Locate every blood parasite and identify its species.
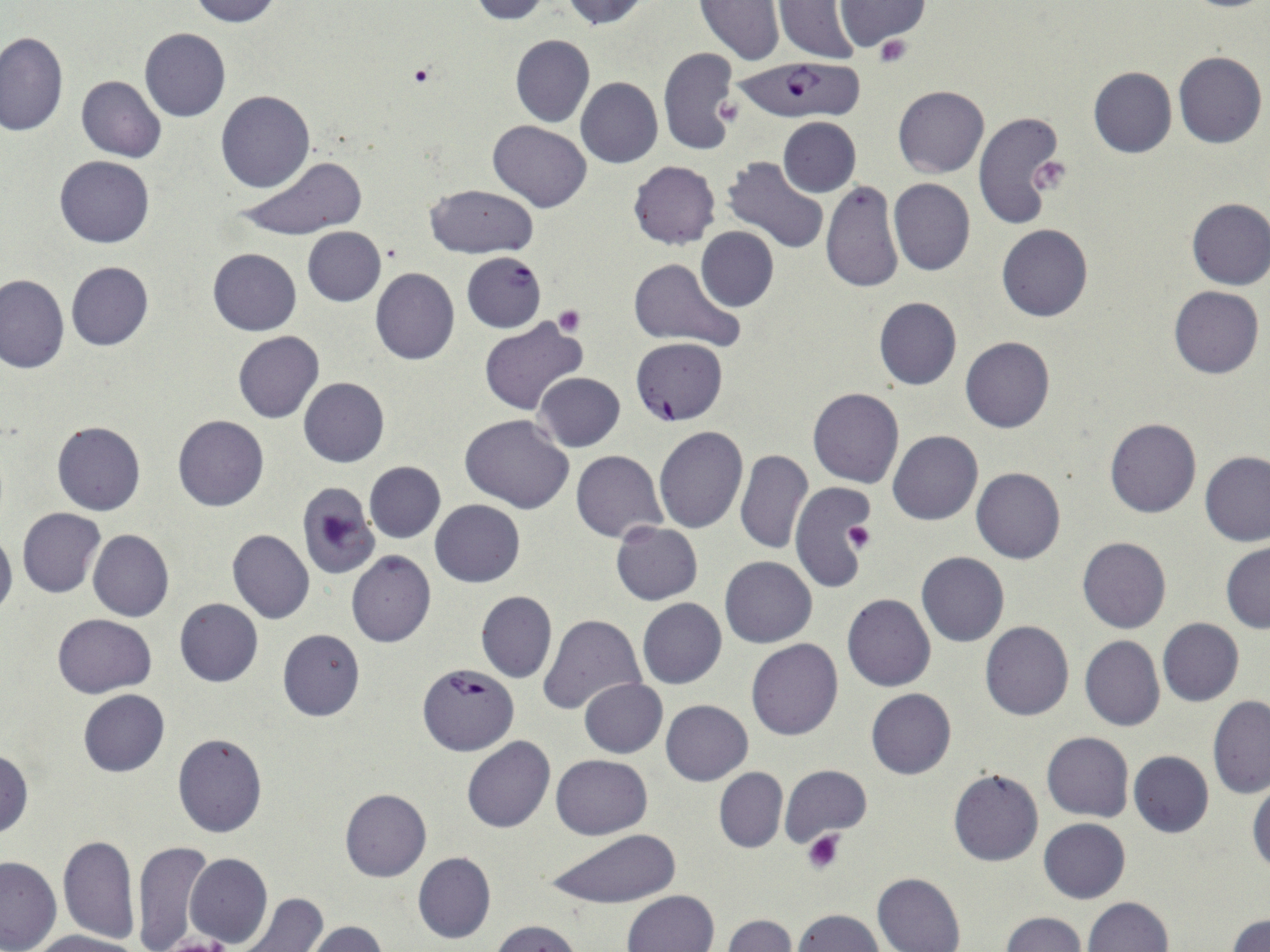
Approximate bounding boxes as (x1, y1, x2, y2) in pixels.
Plasmodium falciparum-infected red blood cells: (733, 57, 869, 131), (462, 251, 546, 333), (631, 337, 727, 425), (420, 665, 517, 754).
No Plasmodium ovale, Plasmodium malariae, Plasmodium vivax, Babesia divergens, or Trypanosoma brucei observed.

Summary:
  - Platelet locations: (875, 33, 914, 68), (407, 64, 439, 89), (1033, 157, 1071, 194), (554, 306, 586, 336), (845, 521, 877, 553), (802, 829, 844, 874), (165, 936, 231, 952)
  - White blood cell locations: (295, 481, 381, 578)
  - Uninfected red blood cell locations: (187, 0, 279, 25), (469, 0, 553, 23), (559, 0, 652, 28), (774, 0, 862, 65), (835, 0, 933, 50), (696, 1, 784, 64), (140, 29, 231, 122), (0, 31, 68, 136), (511, 34, 594, 128), (658, 46, 739, 157), (1173, 50, 1267, 148), (1087, 65, 1176, 158), (76, 76, 165, 161), (576, 77, 664, 169), (893, 85, 988, 178), (216, 90, 314, 192), (972, 109, 1068, 229), (778, 117, 861, 196), (487, 120, 592, 211), (234, 154, 365, 244), (54, 156, 155, 248), (723, 156, 829, 255), (627, 161, 720, 250), (889, 178, 975, 275), (821, 181, 904, 293), (426, 183, 539, 257), (1184, 197, 1270, 290), (997, 224, 1093, 322), (695, 226, 778, 313), (303, 228, 386, 306), (208, 248, 301, 335), (630, 257, 744, 351), (66, 261, 154, 351), (369, 268, 460, 365), (0, 273, 69, 373), (1169, 286, 1263, 379), (873, 297, 961, 390), (479, 318, 589, 418), (233, 331, 323, 423), (961, 337, 1055, 433), (533, 372, 625, 452), (298, 376, 389, 467), (808, 388, 904, 488), (461, 414, 574, 515), (173, 415, 268, 512), (1105, 417, 1201, 519), (52, 421, 145, 516), (654, 425, 749, 532), (888, 430, 983, 525), (735, 449, 810, 554), (571, 450, 667, 541), (1199, 451, 1269, 546), (759, 455, 858, 577), (364, 461, 445, 542), (972, 467, 1066, 564), (788, 482, 876, 591), (431, 500, 525, 586), (18, 507, 106, 597), (611, 521, 702, 605), (0, 526, 17, 621), (88, 529, 173, 622), (226, 529, 315, 623), (1077, 537, 1171, 634), (1221, 542, 1270, 634), (347, 551, 435, 647), (917, 552, 1009, 647), (719, 556, 816, 647), (476, 590, 556, 684), (843, 594, 935, 691), (637, 598, 727, 689), (174, 599, 263, 687), (53, 614, 156, 697), (538, 615, 645, 716), (1158, 618, 1244, 706), (980, 621, 1075, 721), (277, 629, 365, 722), (1080, 636, 1164, 732), (747, 639, 844, 740), (579, 678, 666, 757), (867, 688, 956, 780), (77, 689, 169, 776), (1207, 696, 1270, 798), (661, 700, 753, 785), (1042, 732, 1133, 822), (172, 733, 267, 837), (463, 735, 555, 832), (0, 749, 33, 839), (1129, 751, 1213, 837), (551, 753, 653, 839), (779, 765, 871, 846), (714, 768, 788, 852), (948, 768, 1043, 867), (1249, 781, 1270, 879), (339, 789, 431, 882), (1040, 818, 1130, 903), (545, 827, 680, 912), (58, 835, 139, 944), (131, 841, 212, 951), (413, 851, 495, 944), (185, 852, 272, 948), (0, 856, 61, 952), (873, 872, 965, 951), (624, 890, 718, 952), (234, 894, 328, 952), (1081, 896, 1173, 952), (793, 909, 884, 952), (1000, 912, 1085, 951), (1229, 912, 1270, 952), (723, 915, 797, 952), (489, 919, 584, 952), (302, 920, 389, 952), (31, 930, 145, 952)
  - Slide-level diagnosis: Plasmodium falciparum
  - Modality: light microscopy
  - Image size: 1270×952 pixels
  - Stain: May-Grünwald-Giemsa
  - Field of view: single
  - Magnification: 1000x
  - Preparation: thin blood film